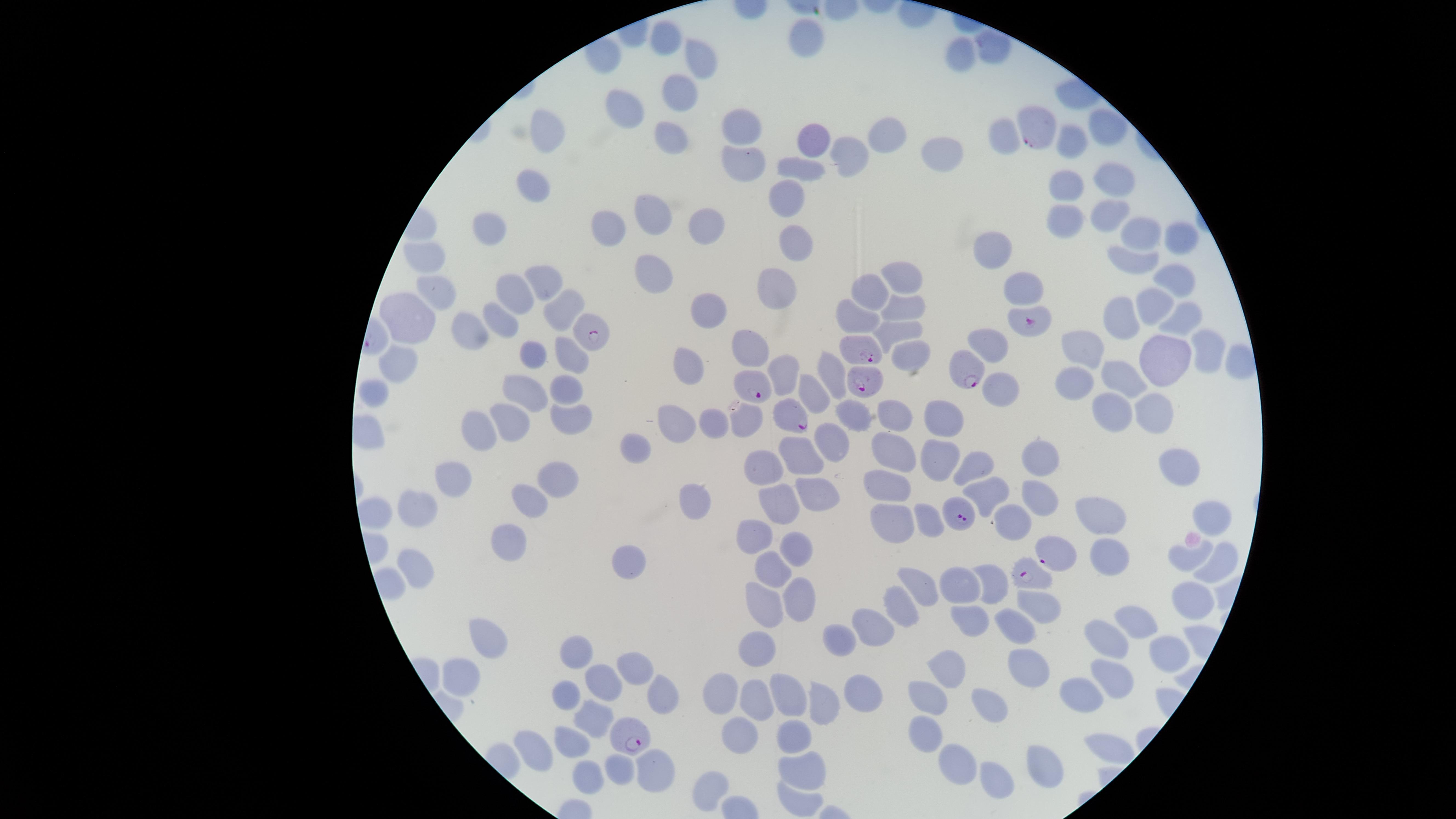

Approximate marker points as [x, y] in pixels.
Summary:
  - Uninfected RBCs: [665, 35], [811, 40], [992, 47], [958, 53], [707, 57], [677, 93], [622, 104], [1103, 124], [744, 128], [549, 131], [669, 131], [885, 134], [814, 138], [1072, 139], [944, 148], [851, 154], [744, 160], [803, 171], [535, 184], [1061, 184], [1110, 184], [785, 196], [654, 215], [1106, 218], [1064, 223], [608, 226], [704, 226], [490, 231], [1135, 235], [797, 239], [1178, 240], [991, 247], [425, 256], [1137, 260], [652, 269], [1174, 274], [548, 280], [902, 281], [435, 285], [776, 285], [1025, 290], [512, 294], [873, 297], [1152, 305], [564, 307], [903, 307], [710, 310], [410, 316], [1120, 317], [1181, 317], [502, 318], [863, 319], [898, 327], [473, 329], [752, 345], [992, 346], [1086, 350], [1208, 351], [908, 352], [533, 353], [569, 356], [1162, 356], [1234, 360], [689, 364], [398, 365], [786, 369], [1117, 372], [835, 373], [1079, 380], [373, 387], [566, 388], [1001, 388], [528, 391], [814, 396], [1144, 405], [1107, 408], [846, 411], [569, 415], [900, 416], [715, 418], [511, 419], [674, 419], [748, 419], [941, 421], [481, 427], [829, 434], [639, 444], [891, 451], [799, 458], [936, 458], [1047, 461], [1188, 464], [973, 468], [768, 469], [454, 482], [559, 482], [888, 491], [812, 494], [983, 494], [528, 497], [1038, 497], [694, 502], [773, 505], [424, 510], [1206, 513], [1102, 518], [930, 520], [890, 521], [1014, 524], [757, 537], [513, 538], [801, 551], [1186, 558], [1107, 561], [1216, 562], [630, 565], [414, 566], [772, 566], [996, 580], [925, 584], [964, 584], [1196, 592], [802, 598], [759, 603], [1046, 604], [898, 605], [969, 616], [1140, 621], [876, 624], [1005, 632], [846, 635], [1111, 639], [485, 645], [760, 649], [578, 653], [1168, 654], [1029, 666], [632, 670], [950, 673], [1113, 675], [461, 676], [607, 683], [857, 685], [727, 690], [662, 694], [931, 694], [568, 696], [791, 696], [989, 696], [1079, 697], [759, 705], [817, 709], [596, 722], [926, 730], [743, 738], [791, 741], [576, 742], [1104, 744], [543, 750], [1032, 765], [961, 766], [805, 768], [624, 772], [653, 772], [588, 777], [1001, 779], [711, 786], [801, 798]
  - Parasitized RBCs: [1033, 128], [1036, 323], [595, 331], [865, 353], [961, 374], [864, 382], [754, 389], [791, 417], [958, 513], [1054, 553], [1029, 577], [632, 737]
  - Image size: 1456×819 pixels
  - Field of view: single
  - Capture: smartphone photograph through the microscope eyepiece
  - Presence: malaria parasites seen
  - Visible region: circular
  - Species: Plasmodium falciparum
  - Stain: Giemsa
  - Preparation: thin blood film